Name the cell type shown.
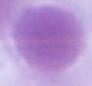

This is an erythrocyte.

{
  "magnification": "1000x",
  "modality": "micrograph"
}